Classify this cell by malaria status.
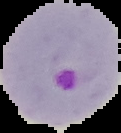

It is parasitized.

The area outside the segmented cell region is set to black. Image is 121×133 pixels. From a thin blood smear.